Name the parasite shown.
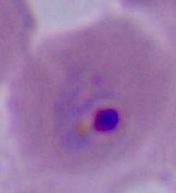
This is Plasmodium.

400x or 1000x magnification. Micrograph.